Locate platelets.
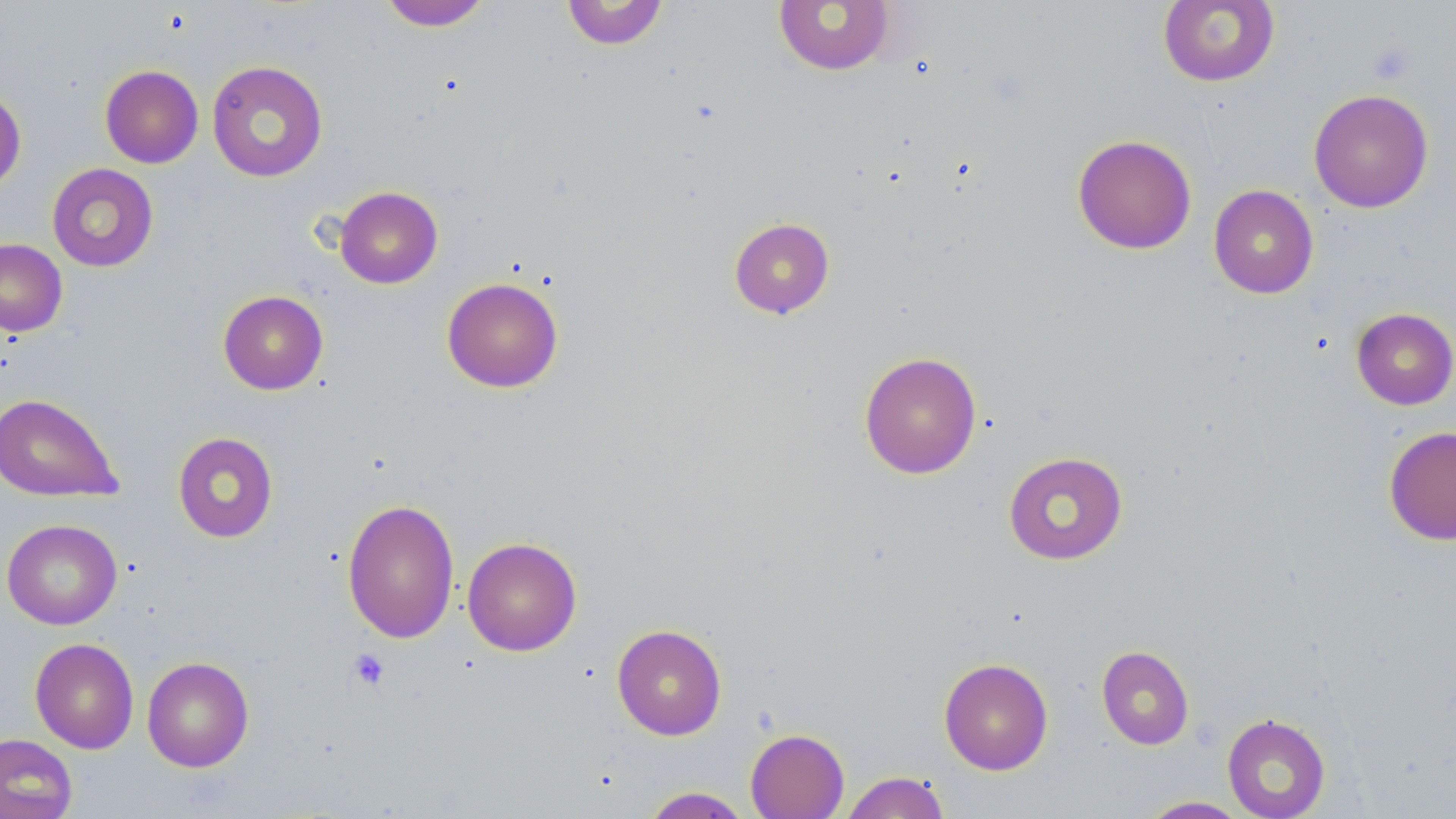
Approximate bounding boxes as named x1/y1/x2/y2 corners in pixels.
Platelets: (x1=1367, y1=43, x2=1416, y2=85), (x1=348, y1=649, x2=390, y2=691).

{
  "slide_level_diagnosis": "no evidence of blood parasites",
  "modality": "optical microscopy",
  "field_of_view": "single",
  "stain": "May-Grünwald-Giemsa",
  "image_size": "1456×819 pixels",
  "magnification": "1000x",
  "uninfected_red_blood_cell_locations": "approximate bounding boxes as named x1/y1/x2/y2 corners in pixels: (x1=560, y1=0, x2=668, y2=50), (x1=1158, y1=0, x2=1280, y2=87), (x1=378, y1=1, x2=493, y2=31), (x1=773, y1=1, x2=895, y2=75), (x1=206, y1=60, x2=328, y2=182), (x1=99, y1=65, x2=203, y2=168), (x1=0, y1=86, x2=26, y2=194), (x1=1308, y1=89, x2=1434, y2=213), (x1=1072, y1=134, x2=1197, y2=254), (x1=47, y1=163, x2=159, y2=272), (x1=1208, y1=184, x2=1319, y2=299), (x1=334, y1=186, x2=443, y2=288), (x1=728, y1=217, x2=835, y2=319), (x1=0, y1=238, x2=68, y2=336), (x1=441, y1=277, x2=564, y2=393), (x1=217, y1=290, x2=328, y2=395), (x1=1351, y1=307, x2=1456, y2=410), (x1=858, y1=351, x2=982, y2=479), (x1=0, y1=393, x2=123, y2=503), (x1=1384, y1=426, x2=1456, y2=545), (x1=172, y1=431, x2=278, y2=542), (x1=1003, y1=451, x2=1128, y2=564), (x1=341, y1=498, x2=460, y2=644), (x1=2, y1=518, x2=122, y2=630), (x1=462, y1=536, x2=582, y2=656), (x1=611, y1=623, x2=727, y2=740), (x1=30, y1=637, x2=139, y2=754), (x1=1096, y1=645, x2=1194, y2=750), (x1=142, y1=656, x2=254, y2=772), (x1=938, y1=658, x2=1054, y2=775), (x1=1222, y1=713, x2=1331, y2=819), (x1=745, y1=728, x2=849, y2=819), (x1=0, y1=733, x2=78, y2=819), (x1=840, y1=771, x2=951, y2=818), (x1=639, y1=786, x2=752, y2=818), (x1=1137, y1=796, x2=1251, y2=818)",
  "preparation": "thin blood smear"
}